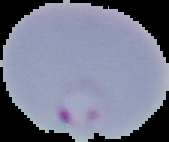
image size = 169×142 pixels
result = Plasmodium parasites detected
preparation = thin blood film
image type = segmented cell region on a black background